Report the malaria status of this cell.
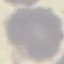
Uninfected.

stain = Giemsa
preparation = thin blood smear
image type = automatically extracted cell patch, resized to 64 × 64 pixels
capture = smartphone camera at the microscope eyepiece